Identify the blood parasite species.
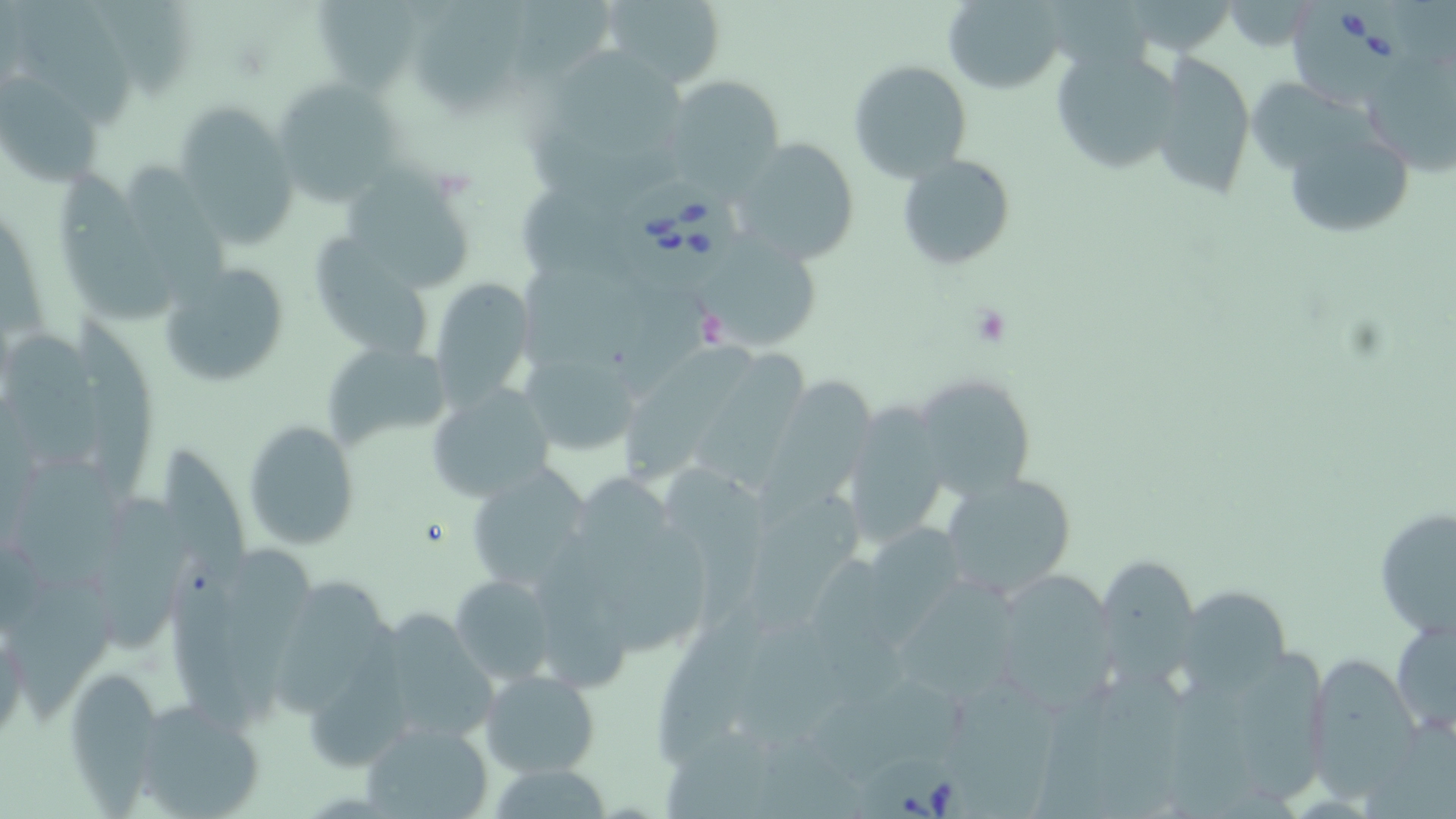

Babesia divergens.

field of view = one of a larger specimen
modality = optical microscopy
stain = May-Grünwald-Giemsa
uninfected red blood cell locations = approximate bounding boxes as [x1, y1, x2, y2] in pixels: [417, 0, 532, 111], [599, 0, 726, 88], [942, 0, 1066, 93], [318, 1, 423, 92], [13, 2, 136, 130], [1051, 47, 1182, 175], [551, 50, 695, 152], [1149, 51, 1255, 199], [1368, 52, 1456, 183], [849, 59, 971, 181], [0, 74, 99, 189], [662, 76, 784, 188], [271, 77, 404, 206], [175, 105, 299, 248], [1282, 125, 1416, 238], [730, 137, 860, 265], [896, 154, 1017, 270], [122, 160, 229, 289], [62, 173, 184, 324], [344, 173, 480, 296], [700, 230, 824, 348], [317, 235, 428, 352], [156, 260, 296, 390], [432, 276, 535, 409], [75, 324, 156, 504], [16, 329, 96, 479], [323, 341, 453, 450], [625, 348, 767, 483], [528, 362, 643, 465], [911, 371, 1036, 500], [768, 374, 880, 496], [427, 386, 557, 501], [838, 401, 951, 549], [243, 419, 359, 549], [161, 444, 264, 597], [465, 462, 596, 596], [663, 470, 779, 627], [938, 472, 1076, 599], [89, 485, 192, 657], [748, 485, 876, 630], [1374, 505, 1455, 642], [601, 515, 722, 659], [870, 520, 982, 650], [223, 547, 320, 736], [1099, 562, 1202, 700], [450, 575, 557, 687], [275, 576, 395, 721], [990, 577, 1118, 719], [890, 581, 1029, 709], [1178, 588, 1297, 700], [365, 607, 498, 749], [654, 609, 771, 764], [1390, 612, 1456, 737], [1153, 638, 1333, 816], [1305, 652, 1426, 801], [63, 666, 167, 803], [480, 669, 601, 778], [128, 699, 267, 819], [359, 719, 495, 819], [484, 763, 618, 818]
image size = 1456×819 pixels
platelet locations = approximate bounding boxes as [x1, y1, x2, y2] in pixels: [970, 303, 1012, 346]
magnification = 1000x
Babesia divergens-infected red blood cell locations = approximate bounding boxes as [x1, y1, x2, y2] in pixels: [1292, 1, 1417, 115], [619, 181, 747, 296], [862, 758, 975, 819]
preparation = thin blood film